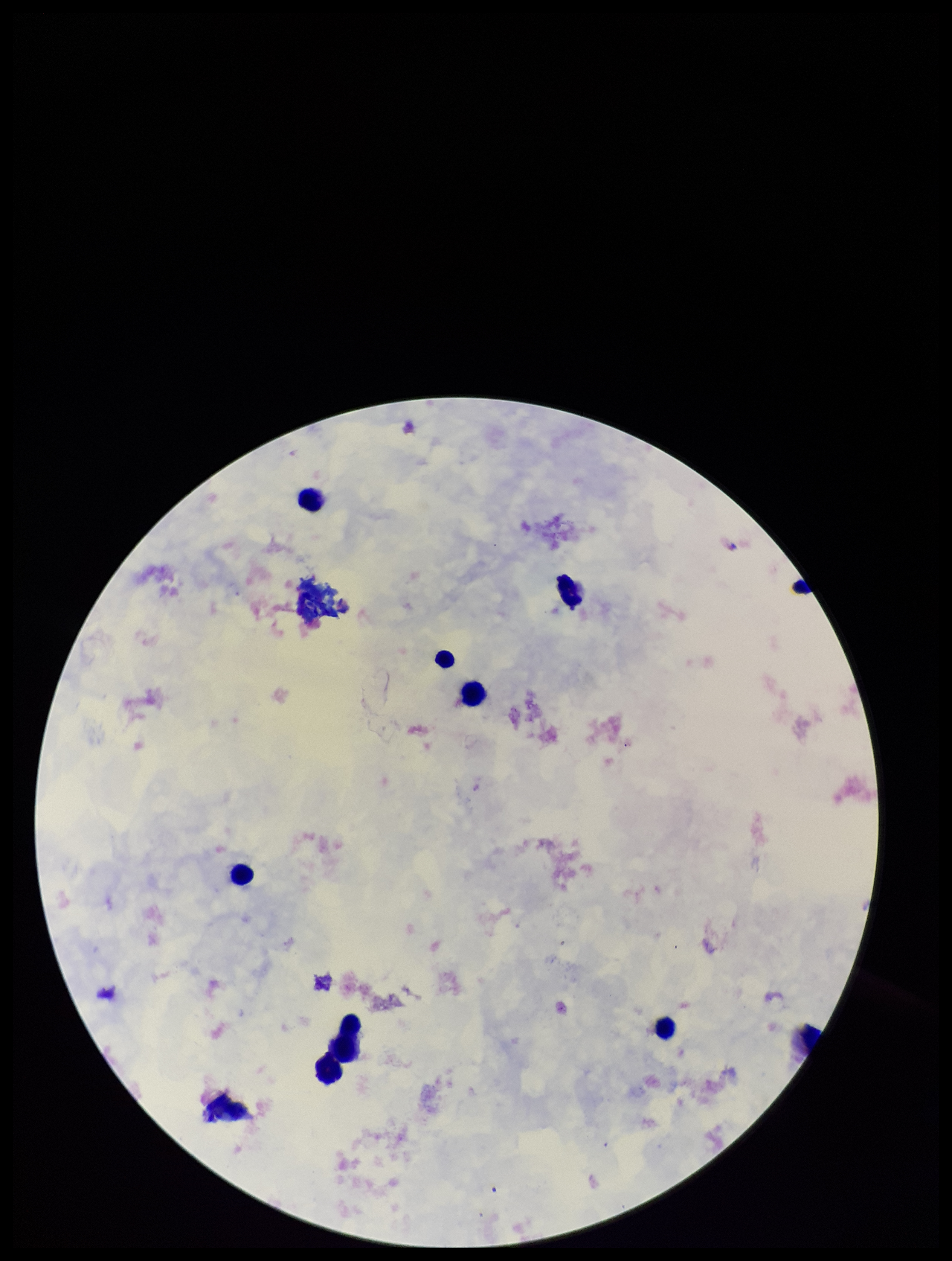 Preparation: thick blood smear. Leukocyte count: 9. Parasite count: 0. Plasmodium parasites: none seen. Stained with Giemsa. Photographed through the microscope eyepiece with a smartphone camera. Image is 952×1261 pixels. Patient malaria status: negative. Single field of view.